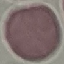 Result: no malaria parasites seen. Photographed with a smartphone camera at the microscope eyepiece. Giemsa-stained preparation. Cell patch, automatically extracted from a larger field of view and resized to 64 × 64 pixels. Thin blood film.